Assess the morphology of the red blood cells.
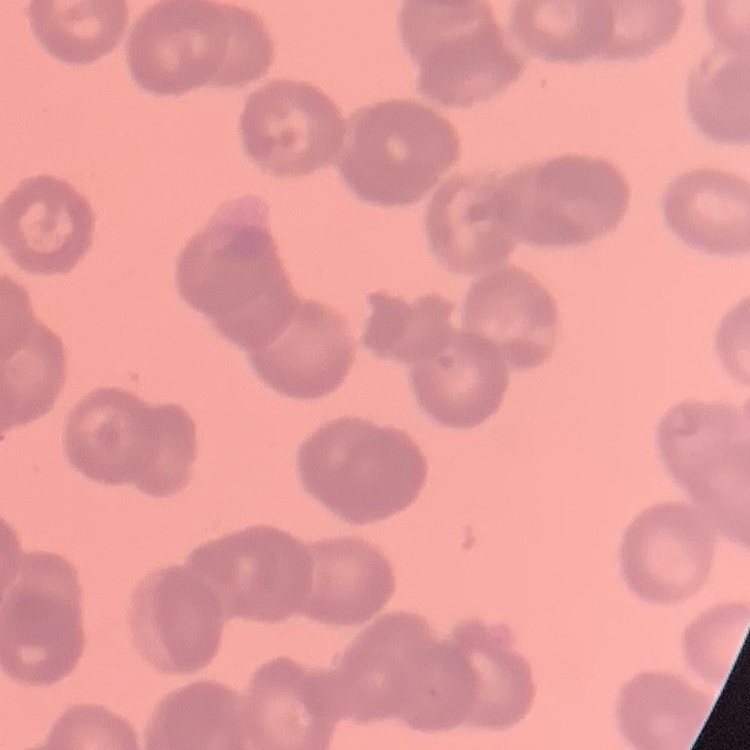

They show rouleaux formation.

One tile cut from a larger photomicrograph. Thin blood smear. Field's or Giemsa stain.